Assess this cell for malaria.
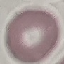

It is uninfected.

Thin smear of blood. Giemsa stain. Acquired by smartphone through the microscope eyepiece. Automatically extracted cell patch, resized to 64 × 64 pixels.